Locate every Plasmodium falciparum-infected red blood cell.
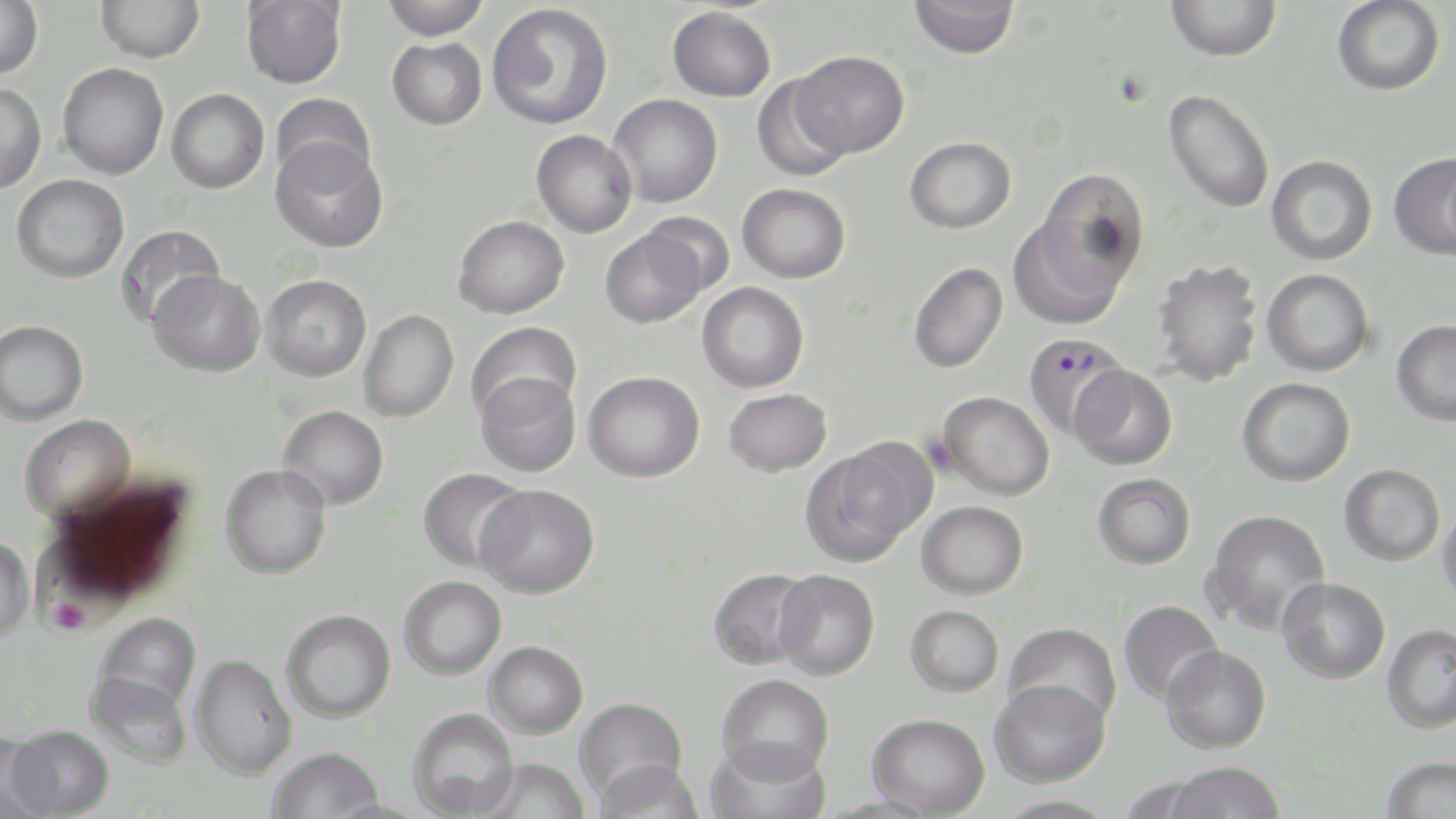
Approximate bounding boxes as (x1, y1, x2, y2) in pixels.
Plasmodium falciparum-infected red blood cells: (1023, 333, 1131, 442).

slide_level_diagnosis: Plasmodium falciparum
preparation: thin blood film
field_of_view: single
platelet_locations: 'approximate bounding boxes as (x1, y1, x2, y2) in pixels: (54, 600, 87, 635)'
image_size: 1456×819 pixels
stain: May-Grünwald-Giemsa
uninfected_red_blood_cell_locations: 'approximate bounding boxes as (x1, y1, x2, y2) in pixels: (0, 0, 43, 78), (96, 0, 205, 63), (241, 0, 347, 89), (382, 0, 490, 41), (909, 0, 1020, 59), (1165, 0, 1281, 62), (1332, 0, 1445, 96), (487, 3, 614, 130), (667, 6, 776, 101), (388, 37, 487, 130), (791, 50, 908, 158), (57, 62, 169, 180), (750, 75, 854, 181), (0, 83, 46, 194), (167, 89, 269, 194), (1164, 89, 1275, 214), (271, 93, 376, 187), (608, 93, 723, 207), (531, 129, 637, 238), (905, 136, 1016, 233), (271, 139, 388, 254), (1389, 152, 1456, 259), (1266, 155, 1377, 265), (1035, 169, 1152, 289), (11, 174, 128, 282), (737, 183, 851, 283), (639, 212, 734, 299), (453, 215, 569, 318), (1007, 216, 1128, 331), (115, 225, 225, 330), (599, 228, 705, 329), (1151, 259, 1264, 387), (908, 262, 1008, 373), (1262, 269, 1374, 376), (148, 270, 265, 377), (261, 274, 371, 381), (697, 282, 809, 393), (359, 309, 459, 422), (0, 320, 88, 425), (1392, 320, 1456, 425), (466, 321, 582, 423), (1070, 364, 1178, 470), (583, 371, 705, 482), (475, 372, 581, 478), (1237, 377, 1355, 486), (723, 387, 833, 477), (937, 390, 1055, 500), (278, 405, 389, 509), (19, 414, 136, 521), (802, 442, 931, 565), (1339, 463, 1445, 565), (220, 464, 332, 579), (417, 468, 531, 572), (1092, 473, 1195, 569), (476, 484, 600, 598), (916, 500, 1028, 599), (1437, 504, 1456, 610), (1203, 508, 1331, 634), (0, 534, 35, 642), (27, 545, 149, 643), (707, 567, 816, 670), (773, 569, 880, 680), (398, 576, 506, 680), (1277, 577, 1390, 684), (1118, 600, 1224, 705), (905, 604, 1004, 697), (281, 609, 396, 723), (96, 612, 202, 710), (1002, 622, 1122, 726), (1381, 624, 1456, 733), (484, 640, 588, 737), (1160, 645, 1271, 754), (190, 653, 297, 779), (85, 670, 192, 768), (716, 673, 834, 780), (989, 678, 1110, 788), (574, 696, 688, 801), (407, 707, 519, 818), (867, 712, 990, 817), (7, 724, 114, 818), (0, 733, 54, 819), (706, 738, 831, 819), (267, 746, 385, 819), (1380, 755, 1456, 818), (595, 757, 705, 819), (474, 758, 590, 819), (1163, 760, 1287, 819), (995, 794, 1121, 819)'
modality: optical microscopy
magnification: 1000x